Give the position of every malaria parasite, noting whether each is a trophozoite, schizont, or gametocyte.
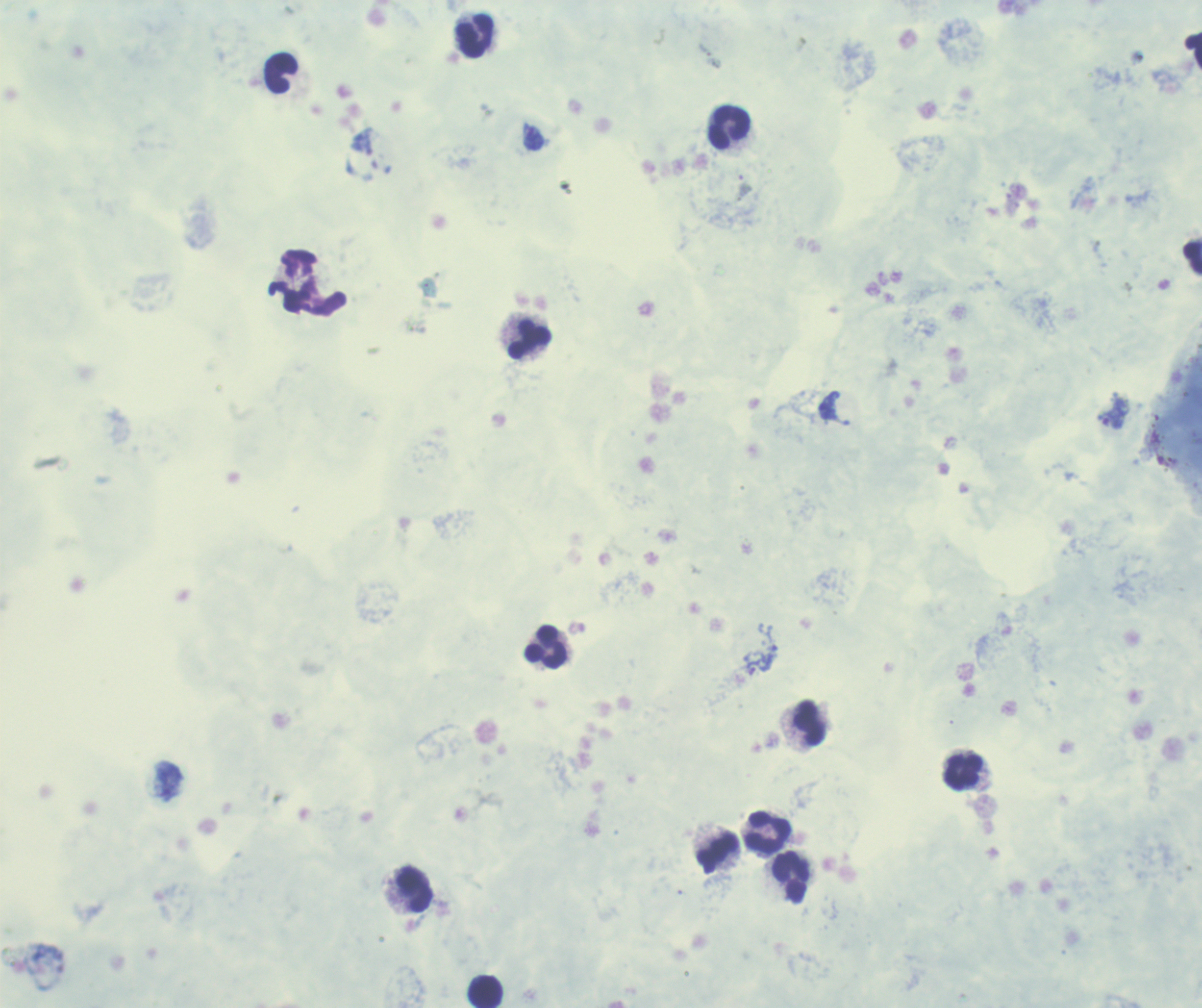
Approximate centers as [x, y] in pixels.
Trophozoites: [533, 137], [829, 405], [1114, 413], [752, 666].
No schizont or gametocyte forms observed.

coordinate format = approximate centers as [x, y] in pixels
leukocyte locations = [475, 35], [1193, 48], [281, 73], [729, 127], [1193, 258], [530, 338], [546, 647], [809, 723], [964, 773], [768, 832], [718, 853], [792, 878], [415, 890], [486, 991]
stain = Romanowsky
magnification = 100x
context = previously used in an actual diagnosis
image size = 1202×1008 pixels
background quality = poor
preparation = thick blood smear
field of view = one from this slide